Give the position of every Plasmodium parasite and every leukocyte.
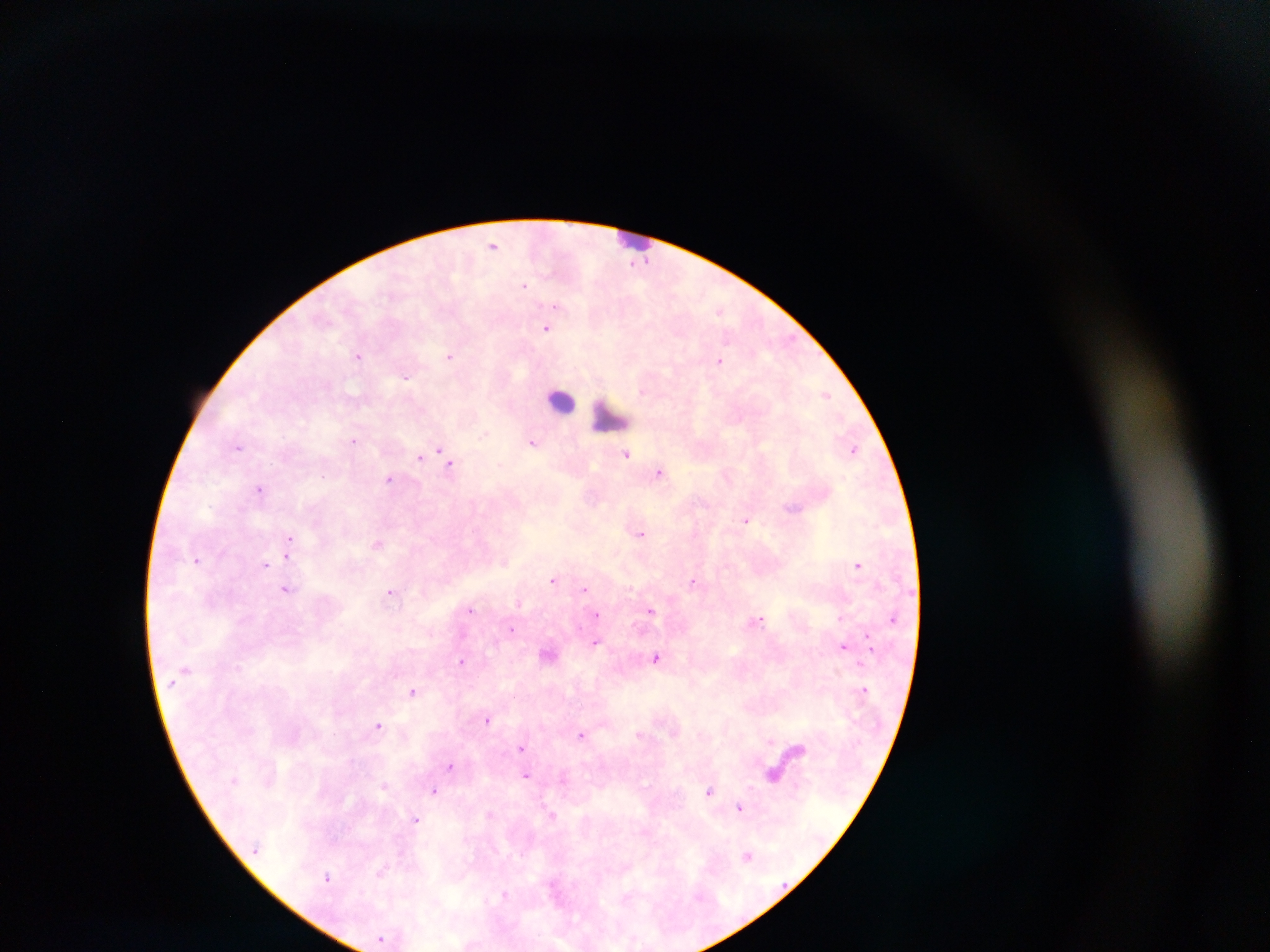
Approximate centers as x y in pixels.
Plasmodium parasites: 494 245; 634 261; 525 286; 547 327; 449 356; 357 357; 718 359; 406 377; 827 394; 485 434; 353 440; 533 442; 438 448; 854 448; 626 454; 419 458; 450 465; 661 472; 389 480; 260 490; 791 510; 747 519; 640 533; 290 537; 289 556; 196 561; 859 564; 265 566; 552 580; 693 582; 585 589; 286 591; 391 591; 519 604; 471 609; 653 612; 597 615; 891 619; 758 620; 512 629; 869 640; 596 642; 845 645; 657 657; 463 662; 837 672; 862 689; 413 692; 488 720; 378 725; 582 735; 771 741; 520 749; 449 766; 526 773; 384 785; 434 790; 709 790; 739 806; 552 814; 490 816; 417 819; 748 854; 329 877; 504 894.
Leukocytes: 628 238; 557 400; 611 413.

Thick blood smear. Collected in Ghana. Photographed through a microscope with a mobile-phone camera. Image is 1270×952 pixels. Single field of view.